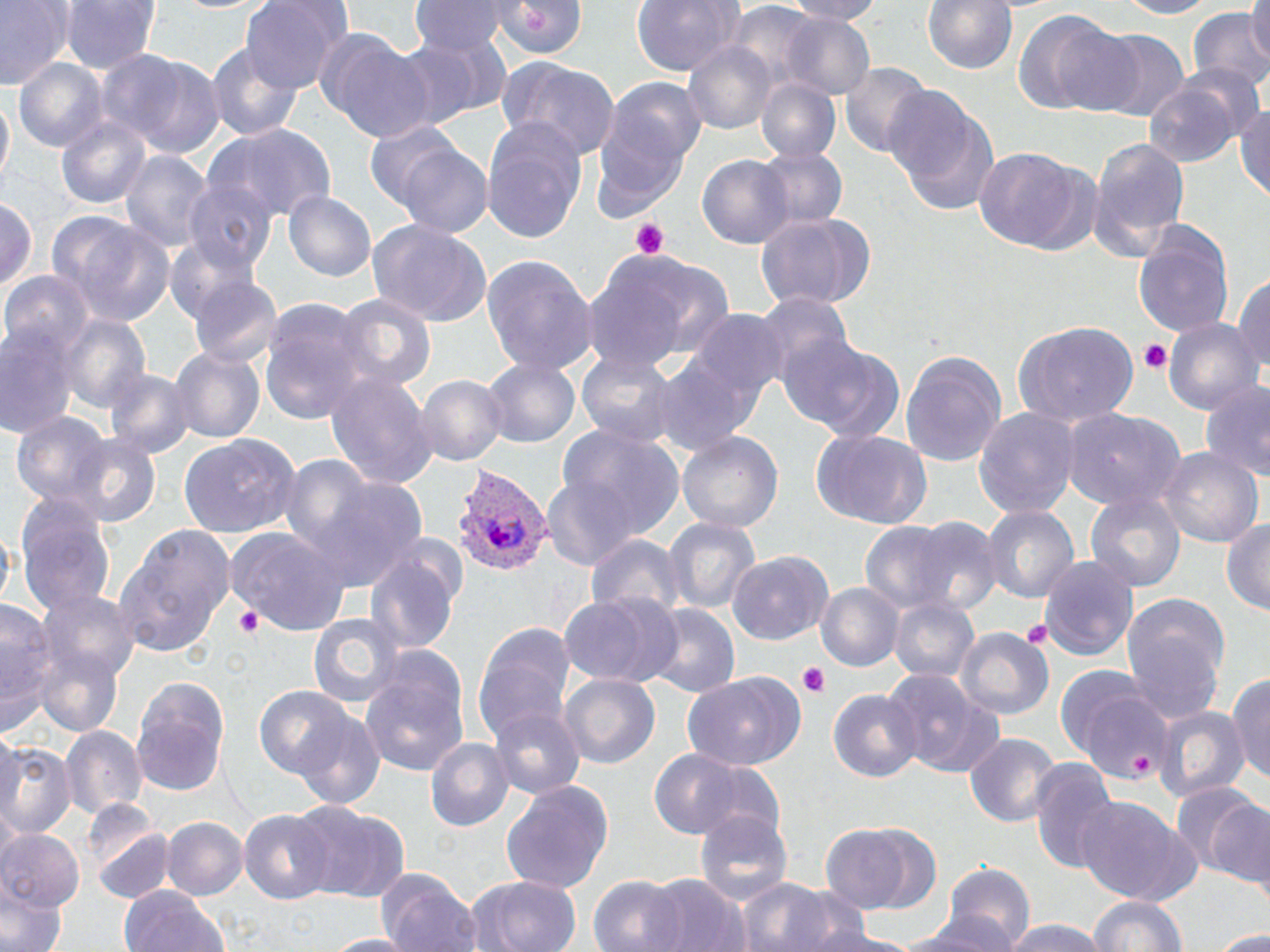
Summary:
  - Coordinate format: approximate bounding boxes as [x1, y1, x2, y2] in pixels
  - Uninfected red blood cell locations: [1, 0, 71, 87], [62, 0, 160, 72], [242, 0, 345, 94], [411, 0, 510, 54], [495, 0, 592, 63], [630, 0, 748, 76], [783, 0, 886, 22], [919, 0, 1019, 73], [1110, 0, 1221, 19], [1247, 0, 1270, 68], [1016, 8, 1128, 118], [1189, 9, 1270, 98], [781, 13, 875, 102], [1087, 29, 1191, 120], [395, 30, 508, 129], [318, 31, 435, 145], [684, 40, 778, 136], [205, 41, 307, 145], [106, 54, 225, 160], [500, 58, 621, 159], [13, 59, 110, 152], [838, 62, 931, 157], [1169, 62, 1266, 149], [755, 77, 842, 164], [1142, 78, 1245, 168], [610, 79, 710, 169], [886, 84, 998, 217], [1, 91, 13, 190], [1237, 95, 1270, 203], [588, 97, 695, 220], [55, 114, 151, 211], [481, 119, 588, 240], [209, 125, 336, 224], [382, 136, 495, 236], [1087, 136, 1191, 263], [756, 146, 847, 230], [972, 147, 1092, 254], [121, 149, 214, 258], [698, 154, 794, 247], [183, 180, 276, 279], [283, 191, 375, 284], [0, 197, 38, 295], [755, 212, 877, 310], [50, 213, 176, 325], [367, 219, 496, 329], [1133, 223, 1233, 334], [164, 235, 266, 333], [590, 249, 734, 368], [481, 252, 593, 375], [1232, 270, 1270, 382], [4, 272, 94, 355], [188, 276, 281, 368], [336, 294, 434, 392], [753, 295, 854, 391], [259, 300, 371, 423], [692, 310, 789, 408], [58, 313, 150, 417], [0, 314, 81, 441], [1163, 316, 1261, 416], [1013, 324, 1140, 427], [779, 337, 903, 442], [984, 344, 1110, 505], [169, 345, 263, 443], [901, 350, 1006, 468], [576, 353, 679, 446], [481, 356, 579, 447], [655, 356, 758, 457], [106, 365, 193, 458], [324, 369, 436, 488], [416, 373, 507, 467], [1199, 382, 1269, 485], [973, 407, 1079, 519], [1061, 410, 1182, 511], [10, 411, 112, 510], [557, 427, 687, 538], [810, 430, 932, 530], [676, 431, 784, 535], [179, 432, 304, 537], [73, 436, 161, 529], [1160, 446, 1261, 550], [280, 455, 376, 557], [314, 476, 431, 593], [539, 476, 638, 566], [1084, 490, 1186, 592], [15, 493, 116, 618], [980, 506, 1076, 603], [664, 516, 760, 615], [871, 516, 1001, 618], [1221, 516, 1270, 618], [112, 524, 231, 659], [227, 526, 349, 634], [586, 532, 689, 617], [728, 551, 833, 644], [364, 554, 459, 659], [1041, 556, 1138, 660], [816, 581, 904, 672], [35, 588, 141, 690], [1118, 590, 1230, 721], [556, 591, 683, 687], [890, 595, 979, 686], [1, 602, 55, 743], [640, 606, 738, 700], [308, 612, 404, 708], [473, 622, 578, 746], [958, 630, 1054, 723], [33, 644, 124, 738], [360, 648, 471, 777], [883, 669, 1005, 778], [1231, 669, 1270, 789], [680, 670, 805, 769], [1063, 671, 1174, 783], [560, 674, 658, 771], [132, 675, 231, 796], [254, 684, 362, 782], [829, 689, 920, 784], [485, 705, 586, 800], [1153, 705, 1248, 803], [292, 712, 386, 812], [60, 726, 146, 824], [963, 733, 1058, 827], [1, 735, 74, 838], [426, 735, 513, 830], [648, 747, 758, 842], [1028, 761, 1118, 876], [502, 781, 616, 891], [1170, 786, 1266, 880], [1073, 799, 1195, 906], [297, 804, 411, 904], [238, 807, 337, 903], [694, 812, 792, 902], [163, 818, 247, 899], [90, 822, 175, 906], [818, 825, 914, 916], [0, 830, 84, 913], [937, 862, 1036, 949], [377, 869, 479, 952], [644, 873, 741, 952], [469, 874, 583, 952], [589, 875, 684, 952], [739, 877, 835, 952], [0, 880, 63, 952], [120, 886, 230, 952], [789, 893, 880, 952], [1087, 893, 1188, 952], [898, 913, 1018, 952], [1000, 920, 1112, 952], [822, 928, 922, 952], [1212, 930, 1270, 951], [320, 933, 416, 951]
  - Plasmodium vivax-infected red blood cell locations: [449, 465, 550, 578]
  - Platelet locations: [629, 218, 671, 259], [1138, 339, 1171, 375], [235, 606, 264, 637], [1018, 622, 1053, 650], [797, 666, 830, 697], [1127, 751, 1159, 776]
  - Slide-level diagnosis: Plasmodium vivax
  - Stain: May-Grünwald-Giemsa
  - Field of view: one of a larger specimen
  - Magnification: 1000x
  - Modality: optical microscopy
  - Preparation: thin blood film
  - Image size: 1270×952 pixels